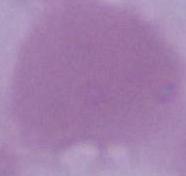
Summary:
  - Modality: photomicrograph
  - Identification: red blood cell
  - Magnification: 1000x